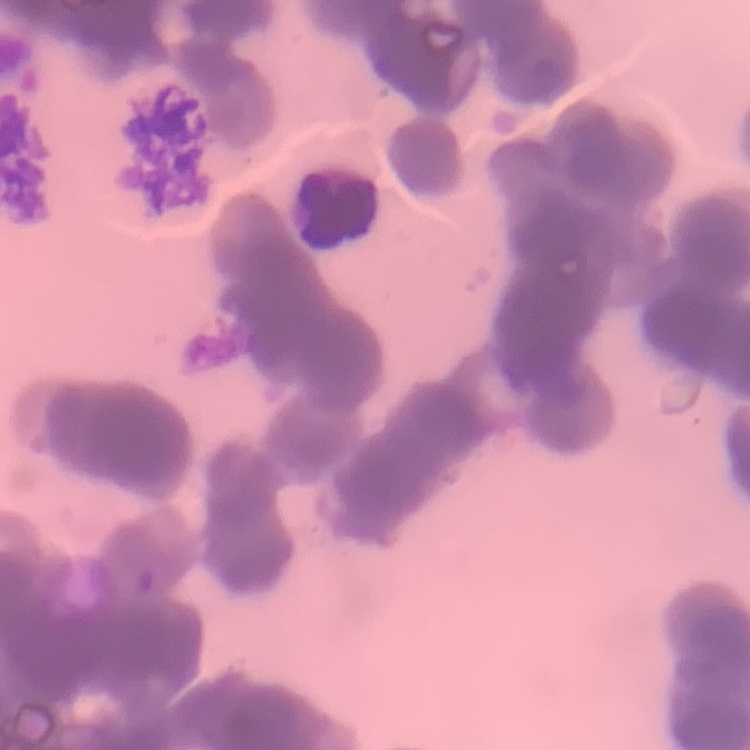
erythrocyte_morphology: rouleaux formation
stain: Field's or Giemsa
preparation: thin blood smear
image_type: one tile cut from a larger photomicrograph